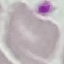 Result: no malaria parasites detected. Thin smear of blood. Giemsa-stained preparation. Photographed with a smartphone camera at the microscope eyepiece. Cell patch, automatically extracted from a larger field of view and resized to 64 × 64 pixels.